Describe the morphology of the erythrocytes.
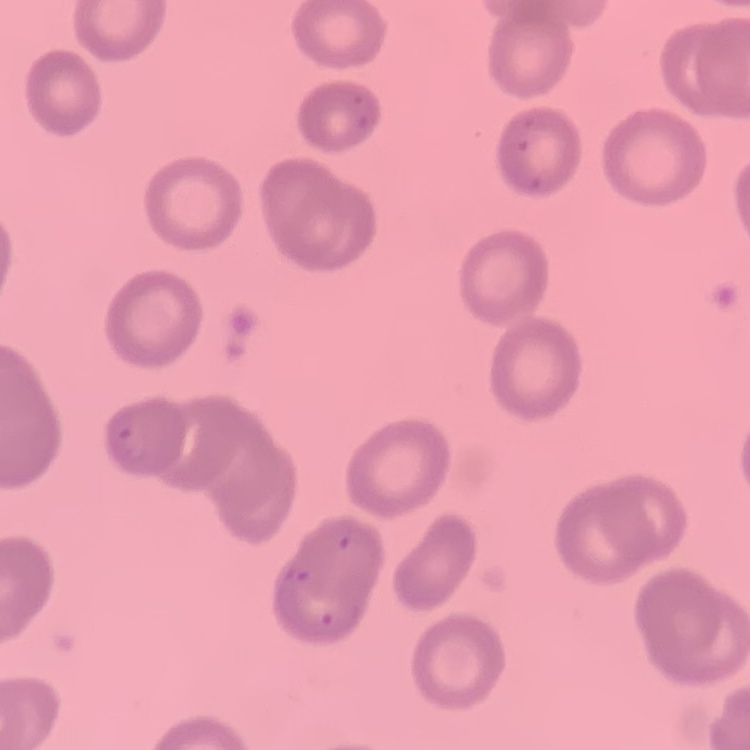
No rouleaux formation.

Summary:
  - Image type: square crop of a larger photomicrograph
  - Preparation: thin blood smear
  - Stain: Field's or Giemsa